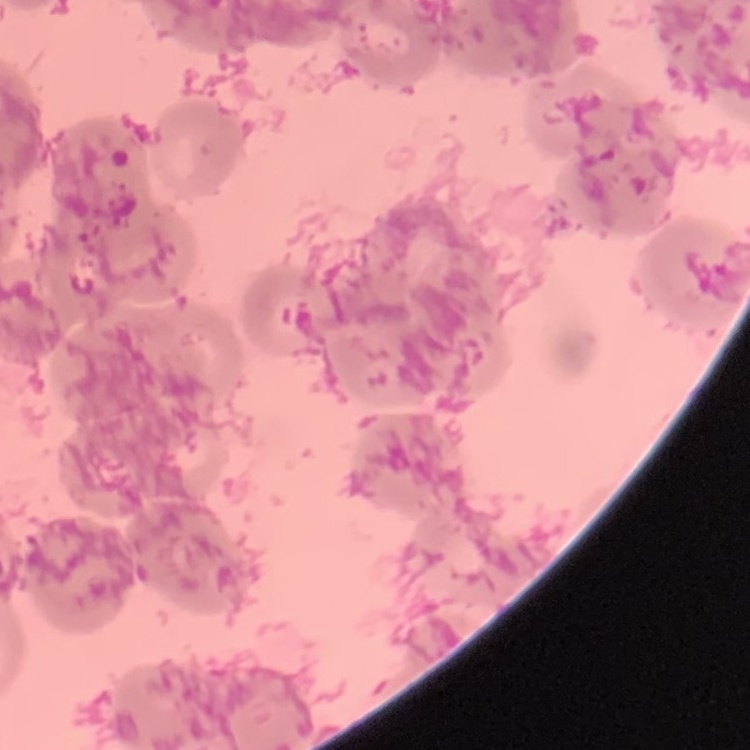
Summary:
  - Red blood cell morphology: rouleaux formation
  - Preparation: thin blood film
  - Stain: Field's or Giemsa
  - Image type: square crop of a larger photomicrograph